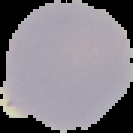
image size = 133×133 pixels
result = no malaria parasites detected
image type = cell region segmented out of the field of view; surrounding area masked to black
preparation = thin blood film